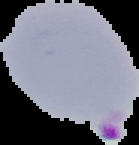
Summary:
  - Malaria status: parasitized
  - Image size: 139×145 pixels
  - Image type: segmented cell region on a black background
  - Preparation: thin blood smear